Give the extent of all uninfected red blood cells.
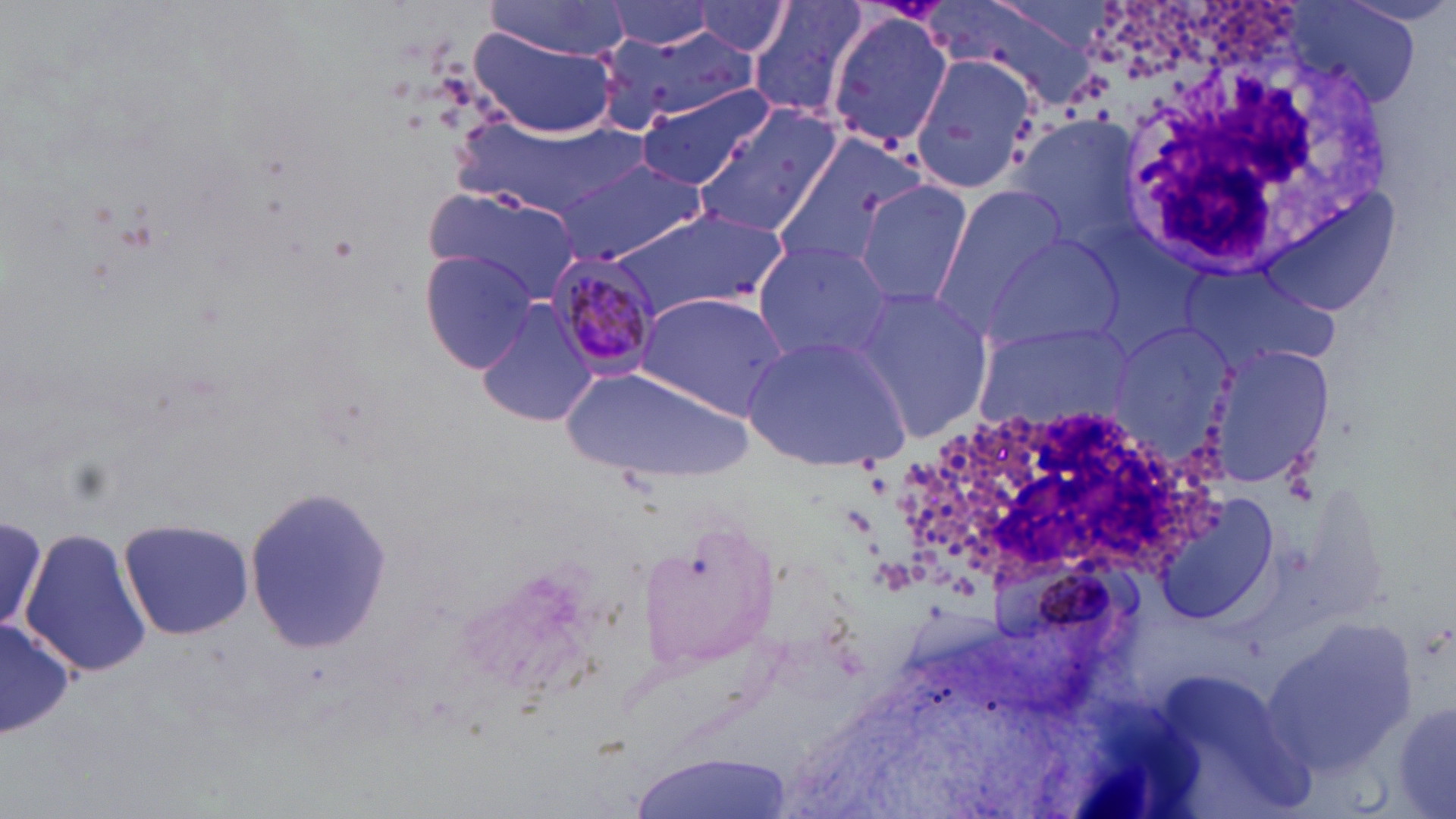
Approximate bounding boxes as [x1, y1, x2, y2] in pixels.
Uninfected red blood cells: [605, 0, 725, 53], [745, 0, 870, 122], [936, 1, 1095, 109], [482, 2, 634, 59], [688, 2, 798, 58], [1286, 4, 1424, 114], [826, 10, 954, 153], [597, 24, 756, 127], [469, 29, 617, 139], [909, 54, 1037, 197], [635, 84, 773, 190], [694, 104, 843, 239], [1007, 113, 1140, 247], [452, 119, 633, 218], [767, 131, 929, 277], [553, 156, 710, 265], [853, 180, 975, 311], [932, 184, 1072, 325], [421, 187, 583, 304], [1254, 195, 1399, 317], [613, 206, 788, 319], [981, 232, 1126, 354], [751, 241, 897, 366], [419, 250, 541, 376], [1176, 260, 1348, 374], [847, 286, 994, 441], [635, 291, 792, 421], [475, 297, 600, 428], [972, 321, 1132, 432], [1103, 321, 1245, 473], [742, 333, 912, 469], [1202, 343, 1334, 493], [561, 365, 753, 486], [243, 485, 392, 653], [1155, 495, 1281, 627], [0, 507, 50, 644], [118, 517, 254, 641], [20, 527, 151, 682], [0, 614, 74, 743], [1260, 617, 1416, 775], [1393, 698, 1456, 818], [630, 756, 789, 819].

Summary:
  - Plasmodium malariae-infected red blood cell locations: [550, 250, 664, 383]
  - White blood cell locations: [1112, 48, 1392, 274], [900, 410, 1220, 585]
  - Slide-level diagnosis: Plasmodium malariae
  - Preparation: thin blood smear
  - Field of view: one of a larger specimen
  - Modality: light microscopy
  - Stain: May-Grünwald-Giemsa
  - Magnification: 1000x
  - Image size: 1456×819 pixels